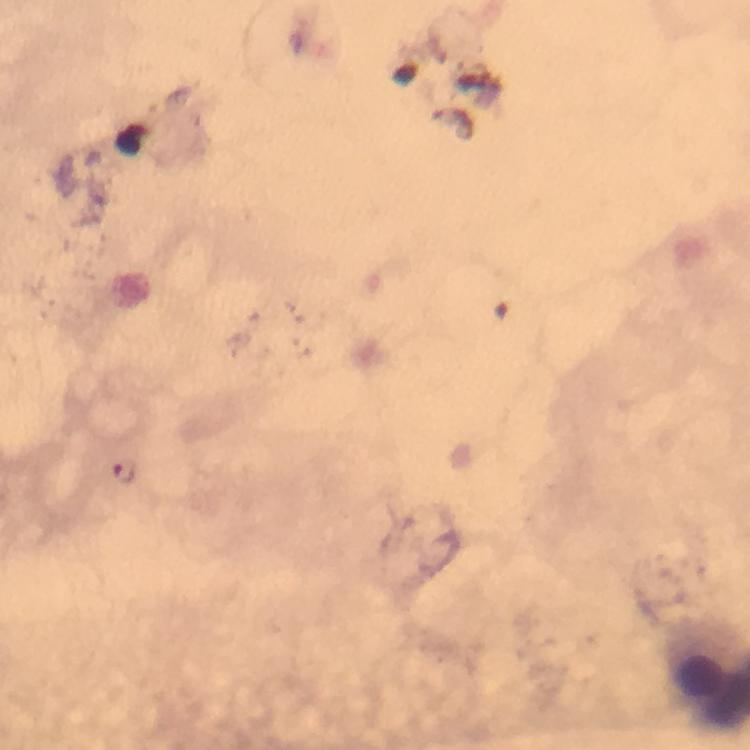

Approximate centers as {x, y} in pixels. Malaria parasite locations: {125, 474}. 100x magnification. Giemsa stain. Immersion oil was used. From a diagnostic examination for malaria. A crop from one field of view. Smartphone photograph taken through a microscope. Thick blood smear. Image is 750×750 pixels.